Report the malaria status of this cell.
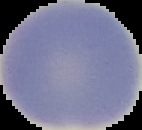
It is uninfected.

Summary:
  - Image size: 142×130 pixels
  - Image type: segmented cell region on a black background
  - Preparation: thin blood smear